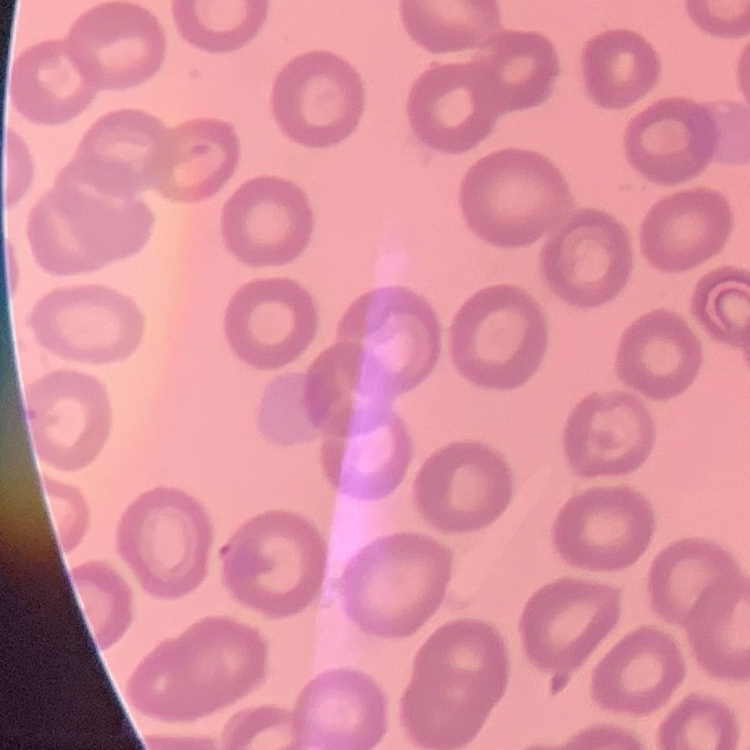
Summary:
  - Red blood cell morphology: no rouleaux formation
  - Stain: Field's or Giemsa
  - Preparation: thin peripheral smear
  - Image type: one tile cut from a larger photomicrograph